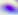
Toxoplasma gondii is shown. Photomicrograph. Captured at 400x magnification.